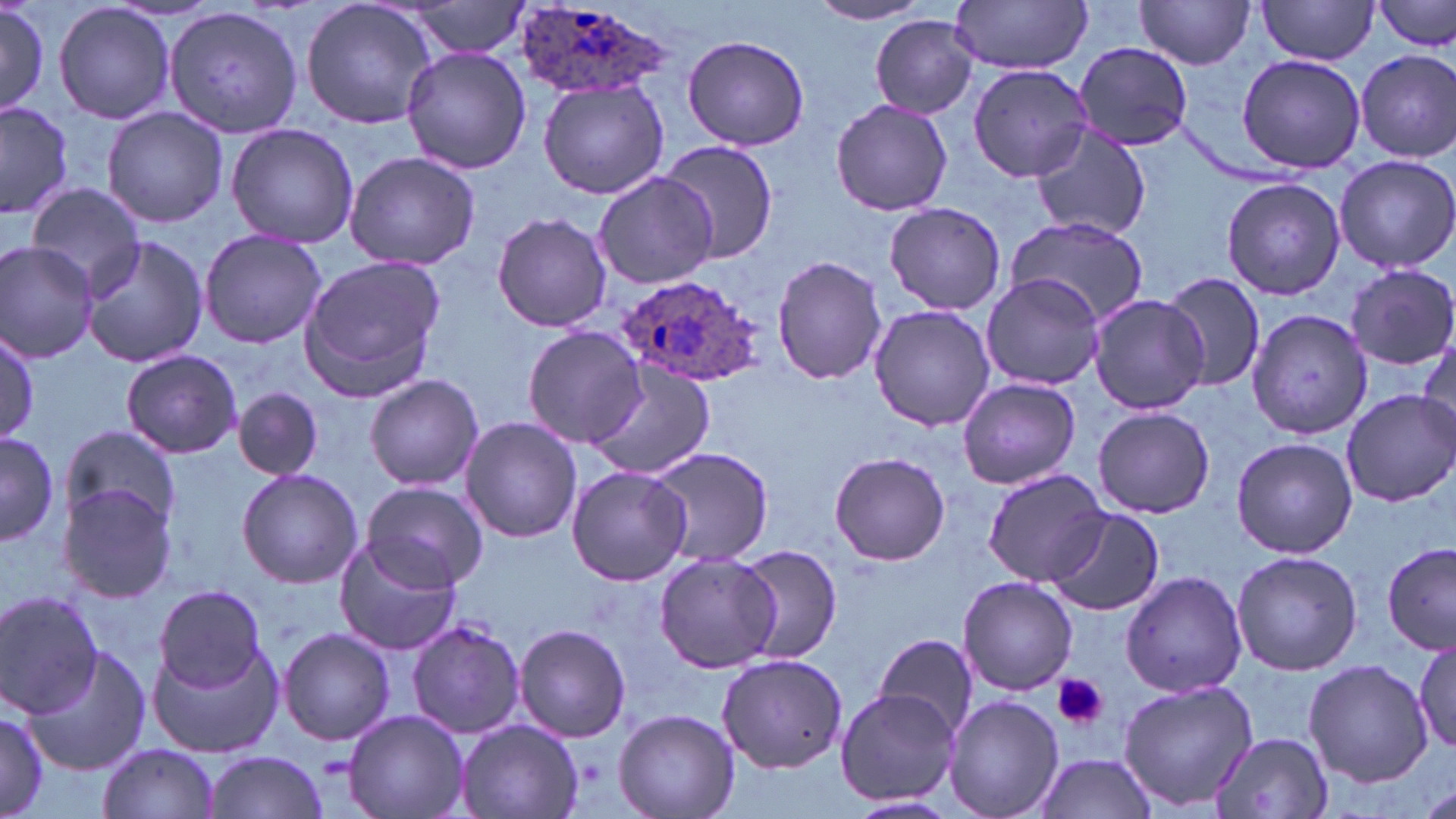

slide_level_diagnosis: Plasmodium ovale
magnification: 1000x
uninfected_red_blood_cell_locations: 'approximate bounding boxes as (x1,y1)-(x2,y2) corner pairs in pixels: (299,0)-(441,130), (1134,0)-(1256,70), (0,1)-(51,121), (398,1)-(535,60), (950,1)-(1092,73), (1256,1)-(1381,64), (1372,1)-(1456,52), (53,2)-(177,126), (808,2)-(931,25), (164,5)-(302,139), (868,15)-(980,118), (684,34)-(809,153), (1073,42)-(1194,150), (399,47)-(531,174), (1353,49)-(1455,162), (1235,53)-(1366,173), (969,64)-(1097,184), (538,80)-(669,201), (830,98)-(953,216), (0,99)-(75,221), (102,106)-(228,229), (1029,122)-(1151,241), (225,123)-(359,249), (658,141)-(779,263), (344,151)-(480,271), (1333,153)-(1456,274), (591,172)-(717,289), (1221,177)-(1346,300), (25,182)-(147,294), (882,202)-(1006,315), (491,211)-(613,333), (1006,217)-(1147,324), (198,228)-(328,350), (78,235)-(211,368), (0,239)-(101,364), (773,254)-(887,385), (297,256)-(446,398), (1347,263)-(1456,369), (1161,271)-(1266,392), (980,273)-(1105,388), (1088,295)-(1209,415), (867,304)-(996,431), (1244,309)-(1373,440), (0,325)-(40,447), (522,325)-(649,448), (1417,334)-(1455,444), (121,350)-(242,459), (584,362)-(715,478), (364,373)-(483,491), (957,376)-(1080,490), (234,386)-(323,480), (1341,389)-(1456,506), (1093,407)-(1214,518), (459,417)-(583,543), (58,429)-(180,529), (0,431)-(60,546), (1231,435)-(1357,560), (646,445)-(773,567), (829,451)-(951,566), (566,465)-(692,586), (236,468)-(365,590), (984,468)-(1104,583), (57,480)-(178,606), (362,482)-(487,593), (1046,508)-(1164,617), (333,537)-(462,657), (732,543)-(843,664), (1382,543)-(1456,654), (1231,549)-(1362,677), (652,552)-(779,674), (1120,570)-(1248,699), (958,576)-(1078,694), (155,585)-(265,689), (0,589)-(105,717), (406,618)-(525,740), (514,624)-(631,742), (278,628)-(396,746), (874,632)-(978,740), (144,633)-(285,759), (1412,638)-(1456,754), (22,643)-(152,774), (717,651)-(848,774), (1305,659)-(1432,786), (1119,679)-(1258,813), (836,689)-(960,805), (944,695)-(1063,819), (613,707)-(739,818), (343,709)-(469,819), (0,710)-(50,813), (455,719)-(583,819), (1211,731)-(1334,818), (97,743)-(220,819), (206,750)-(327,817), (1031,752)-(1158,819), (1421,780)-(1455,819), (840,795)-(962,819)'
plasmodium_ovale_infected_red_blood_cell_locations: 'approximate bounding boxes as (x1,y1)-(x2,y2) corner pairs in pixels: (509,4)-(673,101), (616,271)-(769,389)'
modality: optical microscopy
platelet_locations: 'approximate bounding boxes as (x1,y1)-(x2,y2) corner pairs in pixels: (1051,674)-(1108,730)'
field_of_view: single
preparation: thin blood film
image_size: 1456×819 pixels
stain: May-Grünwald-Giemsa